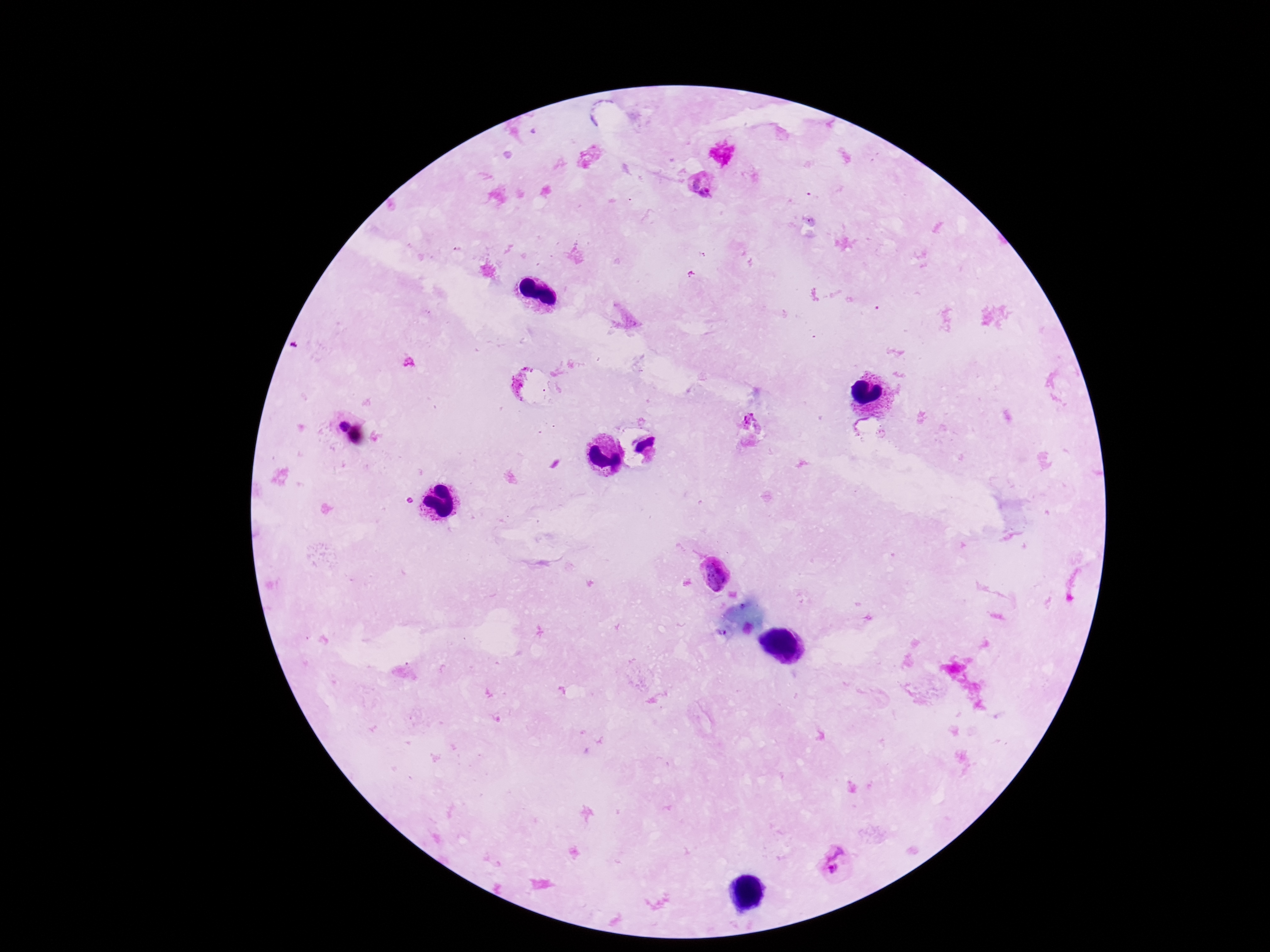

Approximate object centers, in pixels from the top-left corner. Plasmodium parasite locations: (x=702, y=184), (x=335, y=422), (x=752, y=426), (x=716, y=572), (x=834, y=863). Patient malaria status: infected. Single field of view. Image is 1270×952 pixels. Smartphone photograph taken through the microscope eyepiece. Thick blood smear. Giemsa-stained preparation. 100x magnification.